Evaluate for parasitized red blood cells.
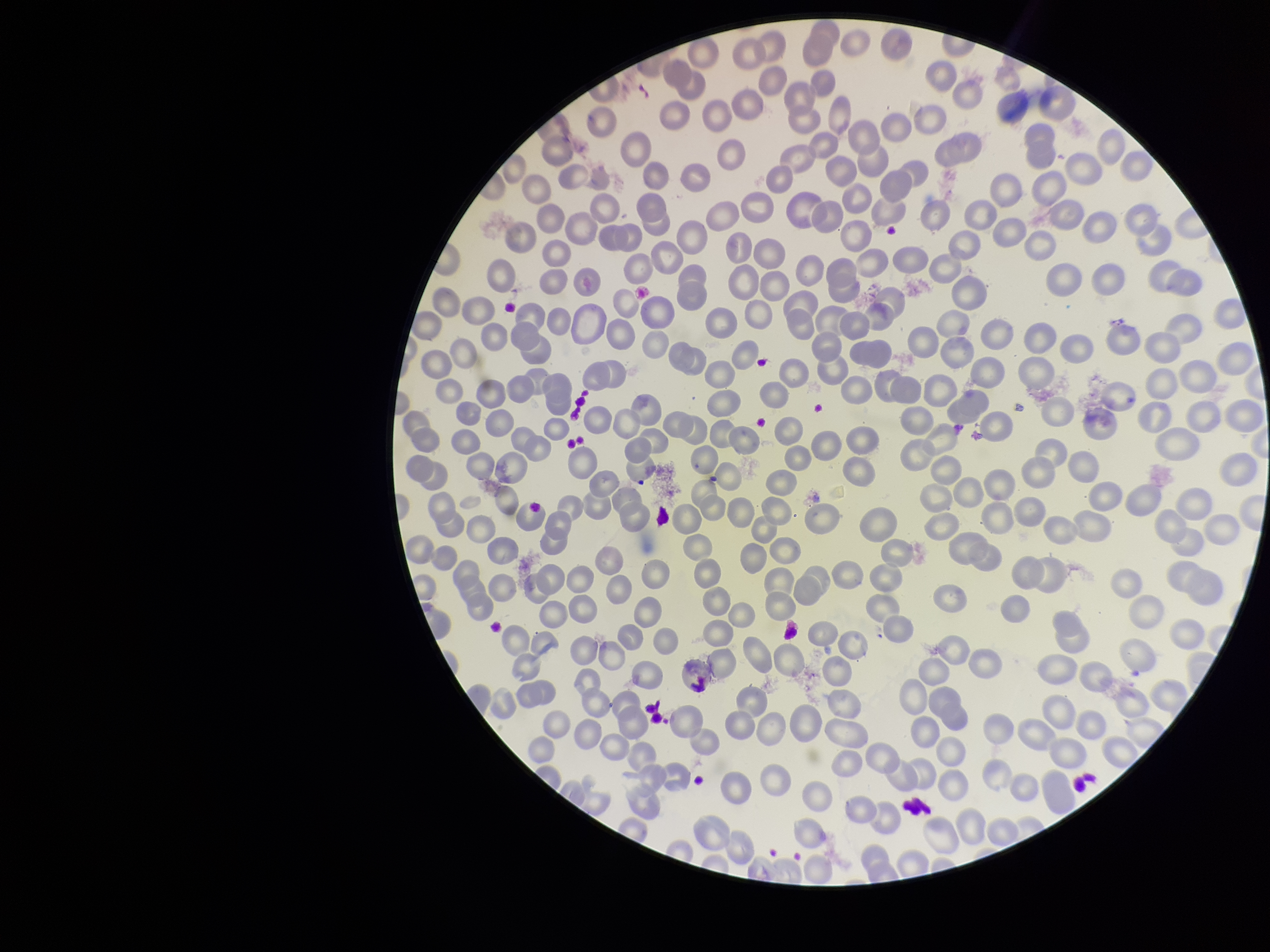
None seen.

{
  "capture": "smartphone photograph through the microscope eyepiece",
  "image_size": "1270×952 pixels",
  "preparation": "thin",
  "parasitized_red_blood_cell_count": 0,
  "patient_malaria_status": "positive",
  "field_of_view": "single",
  "stain": "Giemsa",
  "red_blood_cell_count": 280,
  "species_reported_for_this_patient": "Plasmodium falciparum"
}